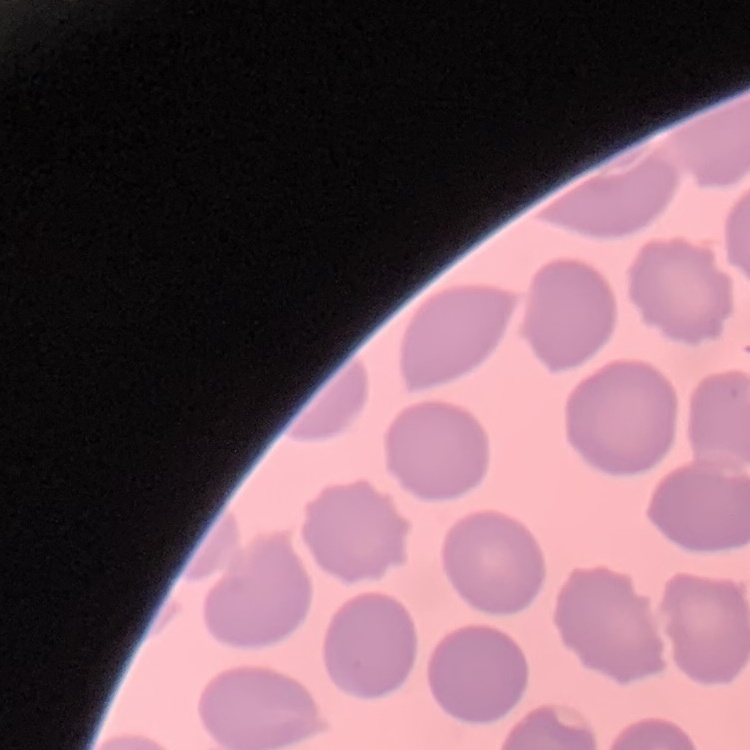
The red blood cells show no rouleaux formation. Square crop of a larger photomicrograph. Thin peripheral smear. Stained with either Field's or Giemsa.